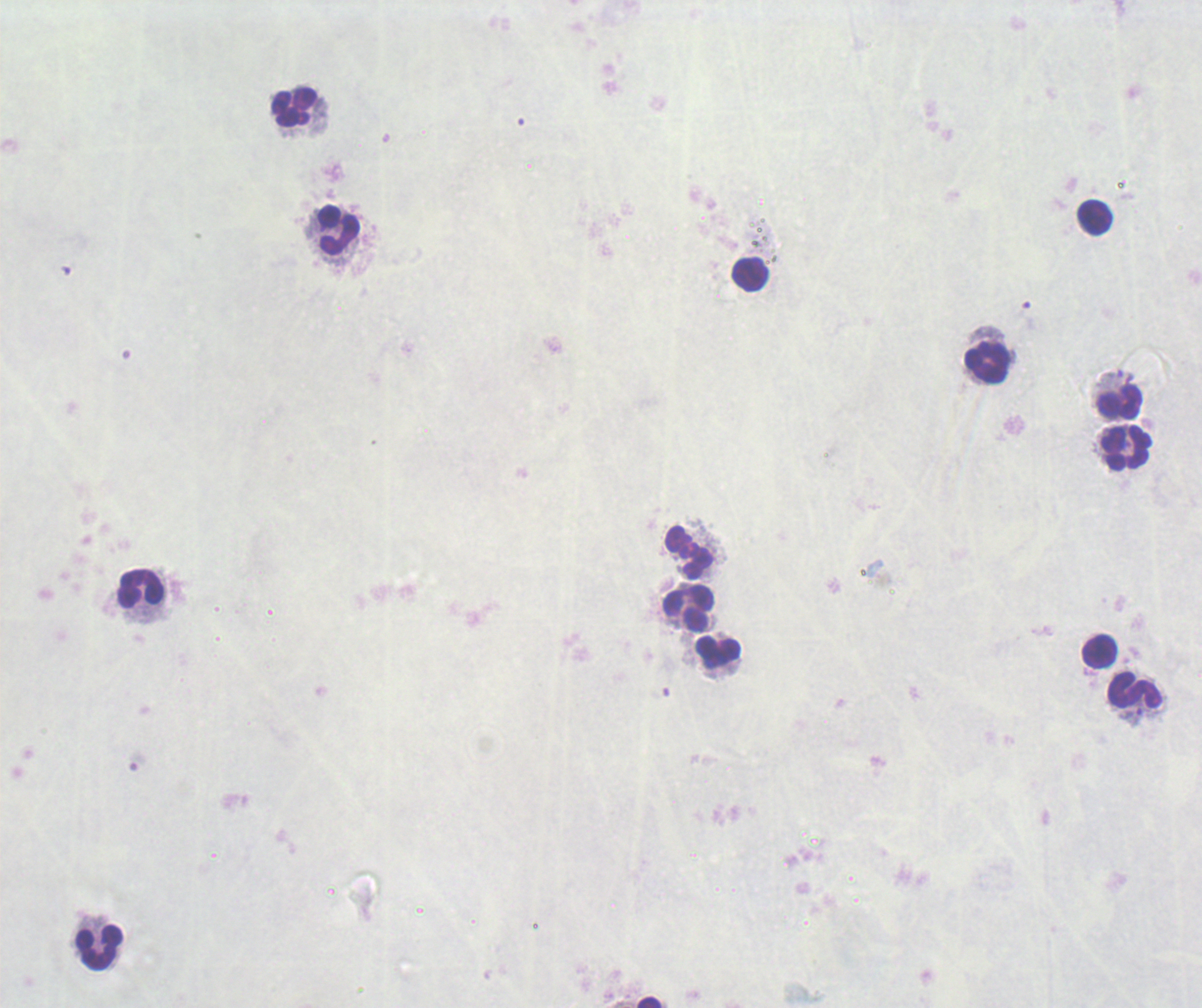
Approximate centers as {x, y} in pixels.
Summary:
  - Leukocyte locations: {294, 107}, {1095, 218}, {339, 229}, {751, 274}, {987, 363}, {1119, 404}, {1127, 450}, {690, 554}, {142, 588}, {689, 609}, {1100, 651}, {719, 652}, {1134, 692}, {99, 948}, {649, 1002}
  - Result: no malaria parasites detected
  - Image size: 1202×1008 pixels
  - Preparation: thick smear of blood
  - Background quality: poor
  - Field of view: single
  - Context: previously used in a real diagnosis
  - Magnification: 100x
  - Stain: Romanowsky